Identify the parasite.
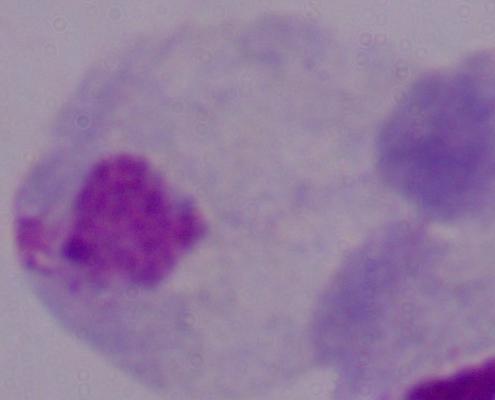
A trichomonad.

magnification = 1000x
modality = micrograph